Assess for malaria.
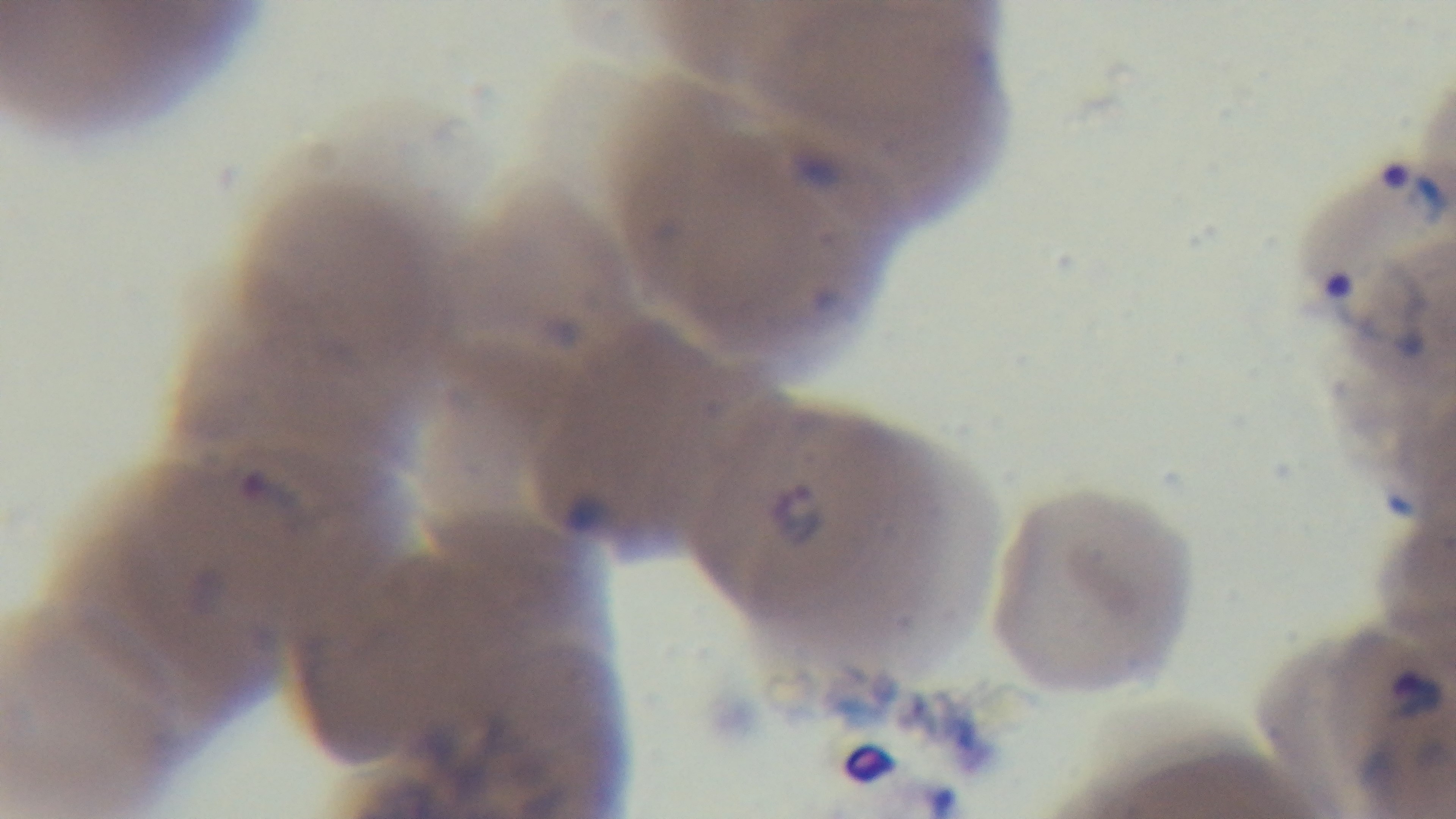
Positive.

field of view = single
modality = light microscopy
objective = 100x oil immersion
preparation = thin
capture = mounted 4K digital camera
stain = Giemsa